Give the position of every malaria parasite and every leukocyte.
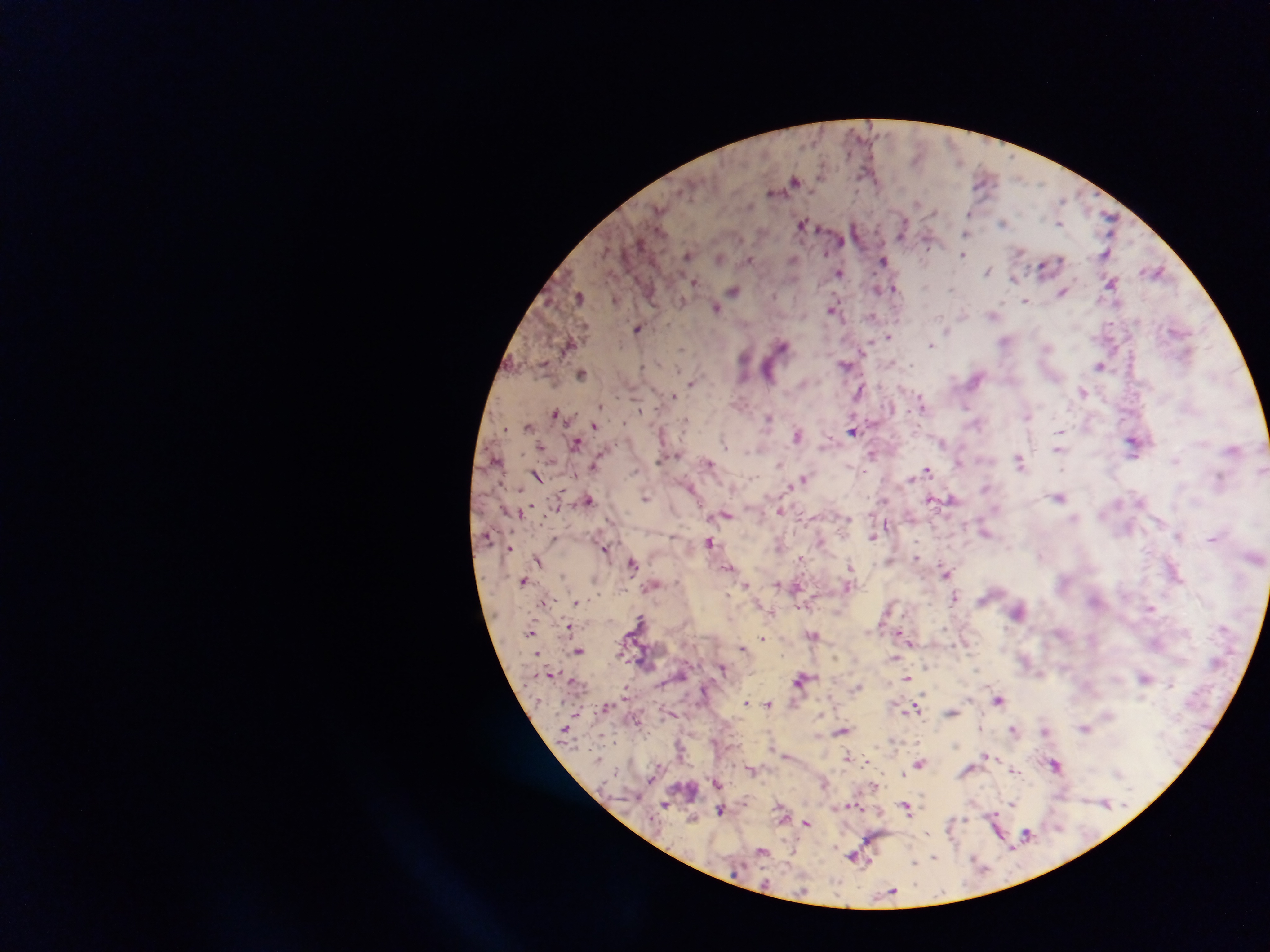

Approximate centers as x y in pixels.
Malaria parasites: 960 162; 794 181; 982 181; 772 192; 1062 199; 919 203; 660 208; 932 212; 969 213; 1108 219; 1002 223; 1060 223; 802 224; 902 228; 966 234; 841 242; 928 243; 1106 253; 963 255; 686 256; 719 258; 793 259; 1060 259; 748 260; 883 260; 1044 267; 988 270; 1155 272; 839 273; 1014 278; 694 282; 1111 282; 895 288; 878 289; 952 289; 733 291; 1062 292; 579 297; 616 300; 1025 301; 682 302; 715 307; 833 309; 993 315; 872 316; 940 317; 638 328; 888 337; 1005 340; 930 344; 781 345; 866 347; 682 349; 743 357; 910 364; 845 365; 1099 365; 768 370; 582 373; 976 378; 691 382; 859 391; 1083 392; 674 396; 922 405; 600 406; 966 407; 640 410; 555 412; 1027 415; 769 419; 529 426; 594 426; 853 430; 1059 431; 797 435; 577 443; 724 443; 943 443; 1133 444; 540 448; 1058 450; 872 454; 1019 461; 961 462; 708 463; 779 464; 594 466; 1063 469; 927 471; 537 475; 1220 476; 804 480; 792 486; 691 487; 985 487; 1059 497; 646 498; 589 499; 951 499; 931 500; 884 501; 780 511; 726 515; 847 519; 986 532; 1178 536; 872 537; 1213 538; 709 542; 510 547; 605 549; 1041 556; 801 557; 916 558; 539 561; 888 561; 633 563; 850 566; 729 567; 946 573; 524 581; 746 584; 777 584; 848 586; 797 587; 955 597; 575 602; 544 603; 1150 608; 1018 611; 640 619; 570 627; 531 632; 898 632; 813 635; 762 637; 911 642; 742 648; 579 651; 895 659; 723 668; 1144 677; 801 678; 907 678; 1170 684; 857 687; 998 700; 746 702; 769 703; 914 708; 952 712; 981 727; 1085 728; 1013 729; 840 731; 1044 731; 848 756; 986 756; 920 764; 1056 764; 751 770; 1015 772; 903 774; 717 783; 824 784; 1105 803; 1012 804; 665 805; 906 806; 721 810; 692 817; 965 821; 807 823; 1027 834; 1012 848; 762 851; 853 857; 934 857; 914 862; 892 892.
No leukocytes observed.

preparation = thick blood film
capture = mobile-phone photograph through a microscope
country = Ghana
field of view = single
image size = 1270×952 pixels